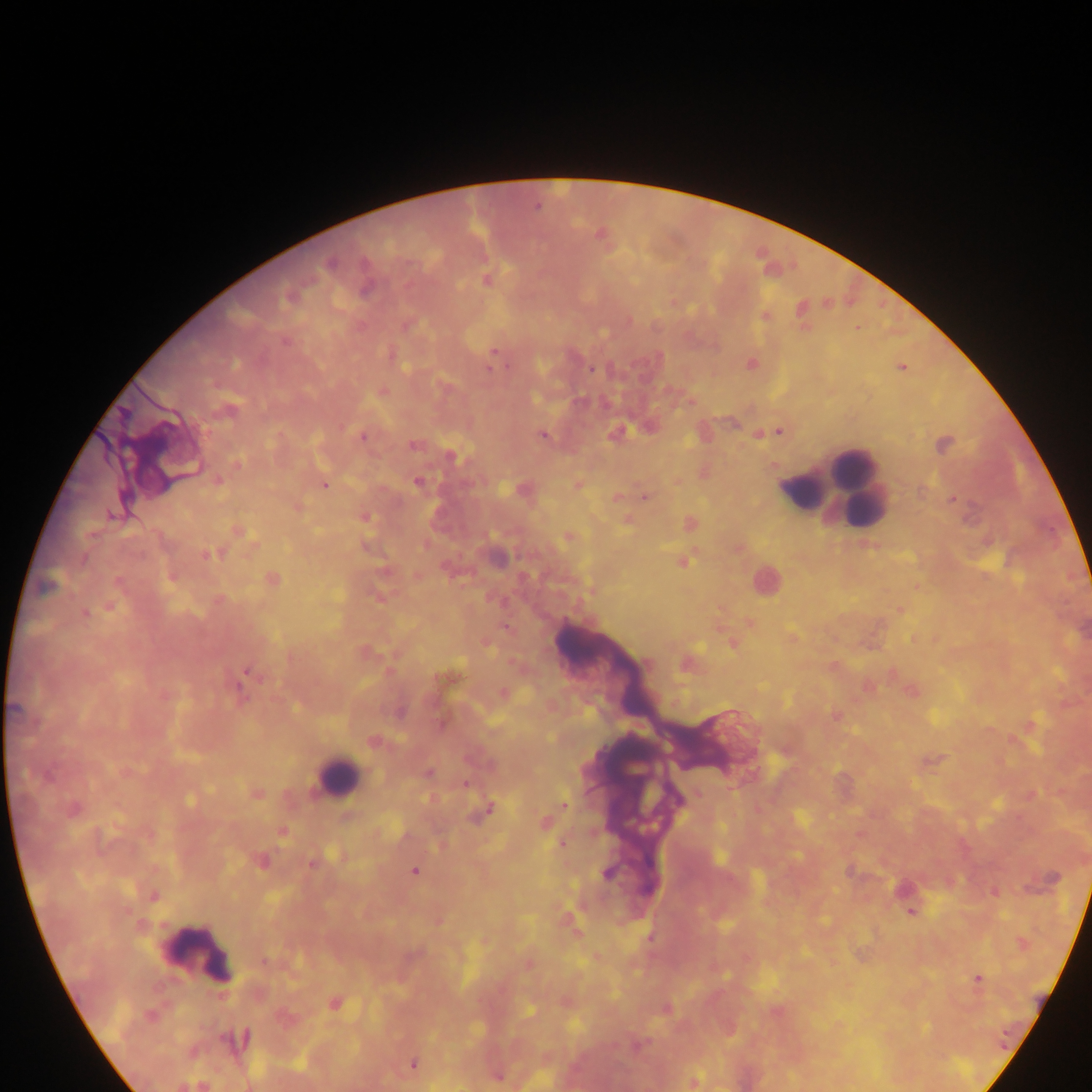

capture: mobile-phone photograph through a microscope
field_of_view: single
image_size: 1092×1092 pixels
preparation: thick blood film
country: Ghana
leukocyte_locations: 'approximate centers as [x, y] in pixels: [852, 467], [829, 487], [803, 491], [766, 580], [336, 775], [199, 953]'
plasmodium_parasite_locations: 'approximate centers as [x, y] in pixels: [536, 207], [601, 235], [329, 263], [486, 281], [766, 316], [285, 341], [494, 352], [491, 362], [488, 368], [591, 369], [382, 392], [229, 411], [779, 431], [616, 433], [544, 435], [363, 437], [414, 445], [450, 457], [238, 464], [218, 480], [417, 482], [324, 485], [577, 485], [645, 497], [953, 499], [111, 516], [365, 518], [238, 531], [569, 537], [210, 554], [683, 562], [273, 578], [45, 587], [110, 606], [86, 613], [750, 624], [732, 644], [647, 663], [247, 672], [238, 689], [836, 716], [429, 772], [465, 785], [258, 793], [190, 800], [564, 805], [74, 809], [490, 810], [545, 824], [282, 833], [563, 844], [262, 862], [311, 864], [415, 871], [607, 874], [153, 896], [910, 912], [264, 961], [979, 978], [335, 1003], [151, 1016], [238, 1040], [638, 1045], [413, 1063], [499, 1077], [694, 1081]'